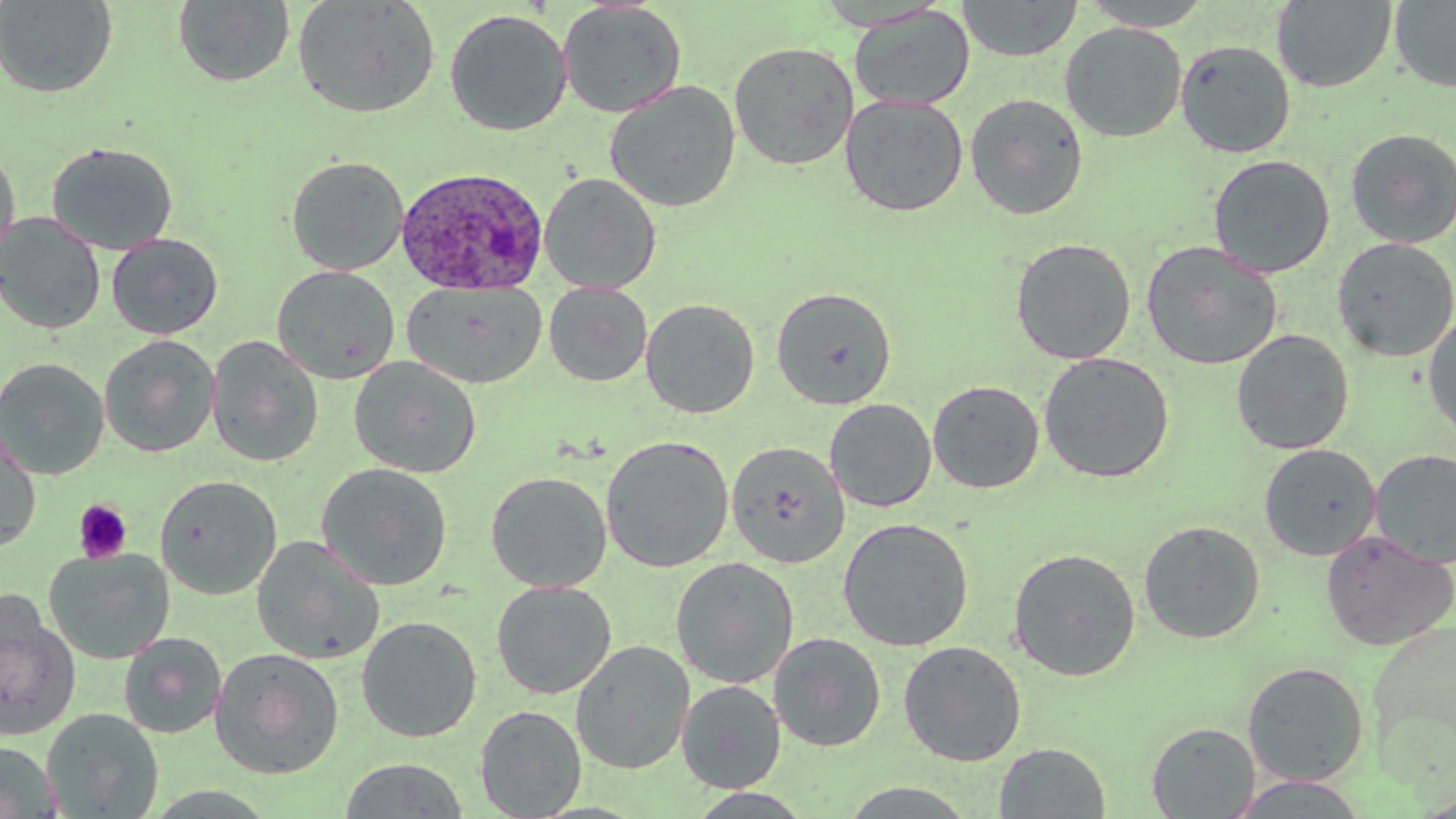

slide-level diagnosis = Plasmodium ovale
image size = 1456×819 pixels
preparation = thin blood film
Plasmodium ovale-infected red blood cell locations = approximate bounding boxes as named x1/y1/x2/y2 corners in pixels: (x1=396, y1=166, x2=548, y2=296)
uninfected red blood cell locations = approximate bounding boxes as named x1/y1/x2/y2 corners in pixels: (x1=0, y1=0, x2=119, y2=98), (x1=293, y1=0, x2=440, y2=119), (x1=958, y1=0, x2=1082, y2=62), (x1=1079, y1=0, x2=1216, y2=30), (x1=1272, y1=0, x2=1398, y2=92), (x1=1390, y1=0, x2=1456, y2=92), (x1=172, y1=1, x2=295, y2=88), (x1=557, y1=1, x2=688, y2=119), (x1=848, y1=4, x2=975, y2=111), (x1=444, y1=9, x2=572, y2=136), (x1=1060, y1=22, x2=1187, y2=142), (x1=1175, y1=39, x2=1296, y2=158), (x1=729, y1=41, x2=859, y2=170), (x1=604, y1=80, x2=742, y2=213), (x1=965, y1=93, x2=1089, y2=220), (x1=840, y1=95, x2=968, y2=217), (x1=1344, y1=127, x2=1456, y2=248), (x1=45, y1=141, x2=179, y2=256), (x1=0, y1=145, x2=20, y2=272), (x1=1208, y1=154, x2=1335, y2=278), (x1=286, y1=155, x2=410, y2=275), (x1=539, y1=173, x2=662, y2=294), (x1=0, y1=213, x2=106, y2=334), (x1=106, y1=233, x2=224, y2=340), (x1=1331, y1=237, x2=1456, y2=362), (x1=1010, y1=238, x2=1137, y2=364), (x1=1141, y1=241, x2=1283, y2=371), (x1=272, y1=265, x2=400, y2=384), (x1=403, y1=281, x2=546, y2=389), (x1=544, y1=282, x2=652, y2=386), (x1=771, y1=286, x2=897, y2=410), (x1=641, y1=298, x2=760, y2=419), (x1=1423, y1=313, x2=1456, y2=443), (x1=1230, y1=329, x2=1355, y2=455), (x1=99, y1=335, x2=219, y2=457), (x1=206, y1=336, x2=324, y2=468), (x1=1038, y1=352, x2=1175, y2=484), (x1=0, y1=357, x2=110, y2=479), (x1=349, y1=357, x2=482, y2=478), (x1=927, y1=379, x2=1045, y2=494), (x1=824, y1=398, x2=937, y2=513), (x1=0, y1=431, x2=42, y2=553), (x1=600, y1=435, x2=735, y2=573), (x1=727, y1=441, x2=850, y2=568), (x1=1258, y1=443, x2=1382, y2=561), (x1=1371, y1=448, x2=1456, y2=569), (x1=316, y1=462, x2=453, y2=591), (x1=485, y1=471, x2=612, y2=592), (x1=155, y1=474, x2=282, y2=599), (x1=838, y1=517, x2=974, y2=652), (x1=1138, y1=519, x2=1266, y2=644), (x1=1320, y1=530, x2=1455, y2=651), (x1=251, y1=536, x2=384, y2=665), (x1=44, y1=546, x2=175, y2=665), (x1=1008, y1=547, x2=1142, y2=681), (x1=671, y1=557, x2=799, y2=688), (x1=491, y1=581, x2=616, y2=700), (x1=0, y1=600, x2=80, y2=742), (x1=356, y1=616, x2=482, y2=743), (x1=1365, y1=619, x2=1456, y2=778), (x1=118, y1=632, x2=227, y2=738), (x1=769, y1=633, x2=886, y2=753), (x1=570, y1=640, x2=695, y2=774), (x1=898, y1=641, x2=1027, y2=767), (x1=209, y1=647, x2=345, y2=779), (x1=1242, y1=661, x2=1370, y2=786), (x1=676, y1=679, x2=786, y2=794), (x1=475, y1=705, x2=587, y2=818), (x1=41, y1=708, x2=164, y2=818), (x1=1146, y1=721, x2=1260, y2=818), (x1=0, y1=741, x2=60, y2=819), (x1=995, y1=742, x2=1111, y2=818), (x1=337, y1=757, x2=470, y2=818), (x1=1227, y1=774, x2=1370, y2=817), (x1=837, y1=782, x2=982, y2=817), (x1=1412, y1=789, x2=1456, y2=818)
modality = light microscopy
platelet locations = approximate bounding boxes as named x1/y1/x2/y2 corners in pixels: (x1=73, y1=499, x2=132, y2=564)
stain = May-Grünwald-Giemsa
field of view = single
magnification = 1000x